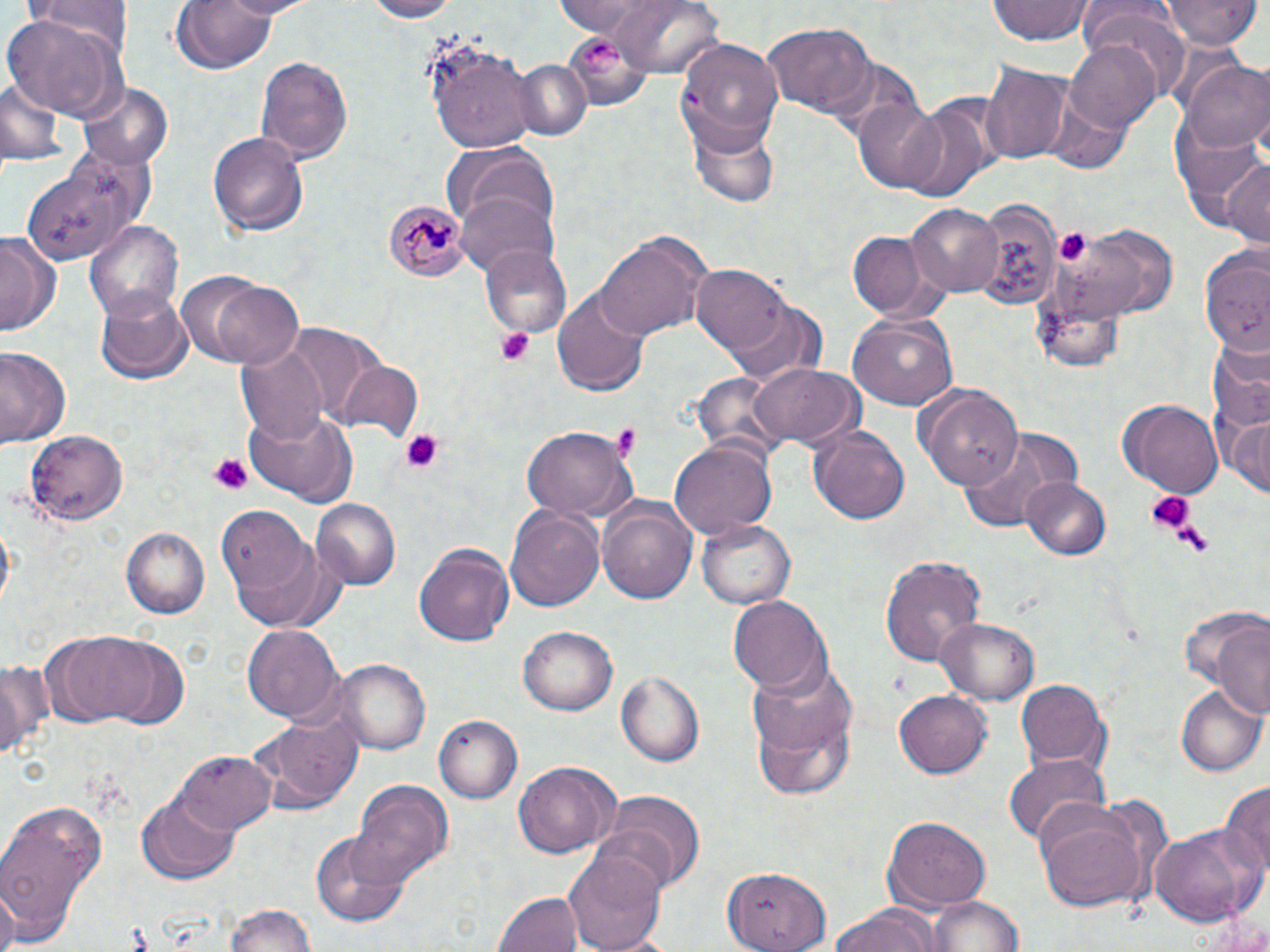
Summary:
  - Coordinate format: approximate bounding boxes as (x1,y1)-(x2,y2) corner pairs in pixels
  - Uninfected red blood cell locations: (29,0)-(128,58), (169,0)-(283,76), (210,0)-(320,19), (358,0)-(458,22), (601,0)-(722,78), (1163,0)-(1260,50), (987,1)-(1096,47), (1077,6)-(1192,89), (7,17)-(127,119), (763,20)-(876,116), (1064,37)-(1163,134), (423,38)-(539,151), (676,38)-(784,156), (255,56)-(354,167), (518,60)-(589,141), (981,61)-(1071,165), (1183,62)-(1270,157), (0,76)-(61,167), (76,77)-(177,170), (852,98)-(949,193), (896,103)-(996,206), (1175,105)-(1268,238), (687,118)-(781,211), (206,128)-(309,236), (448,149)-(563,247), (20,154)-(156,264), (1220,157)-(1269,247), (456,191)-(558,278), (971,200)-(1062,310), (908,205)-(1003,296), (84,220)-(185,327), (1058,225)-(1180,320), (593,227)-(714,342), (848,230)-(932,319), (0,232)-(56,338), (1199,241)-(1270,353), (482,243)-(571,339), (692,266)-(793,355), (213,282)-(305,368), (553,286)-(651,395), (97,288)-(193,384), (722,300)-(827,382), (848,315)-(956,409), (275,323)-(386,422), (237,342)-(328,443), (0,347)-(71,451), (330,360)-(423,441), (748,364)-(864,451), (918,384)-(1025,491), (1123,398)-(1225,496), (241,405)-(359,506), (1224,411)-(1269,500), (805,421)-(909,526), (518,422)-(636,521), (958,428)-(1080,530), (25,429)-(131,524), (669,439)-(776,542), (1022,478)-(1111,561), (597,498)-(697,606), (310,499)-(401,590), (217,505)-(326,627), (505,506)-(605,614), (699,518)-(799,609), (120,525)-(211,617), (416,541)-(515,647), (879,554)-(985,665), (728,595)-(829,694), (1181,603)-(1267,705), (932,617)-(1040,704), (1213,624)-(1269,722), (245,625)-(342,723), (518,625)-(617,715), (48,630)-(162,725), (102,640)-(191,732), (0,658)-(52,762), (333,659)-(432,754), (746,659)-(857,794), (616,672)-(704,766), (1017,678)-(1107,768), (1176,685)-(1267,778), (893,690)-(992,778), (251,711)-(364,815), (434,715)-(521,804), (175,750)-(276,832), (1005,757)-(1109,847), (513,763)-(617,857), (1222,780)-(1270,883), (350,783)-(452,890), (598,791)-(704,894), (138,793)-(240,883), (1035,801)-(1156,913), (0,804)-(106,941), (883,818)-(992,909), (1147,823)-(1263,927), (312,829)-(410,927), (562,846)-(665,952), (724,863)-(829,952), (0,884)-(18,952), (492,889)-(579,952), (925,892)-(1028,952), (220,903)-(318,952), (824,905)-(939,952), (1198,906)-(1269,950)
  - Platelet locations: (582,41)-(626,77), (1062,231)-(1090,266), (495,326)-(536,365), (398,428)-(447,474), (617,428)-(639,459), (208,453)-(252,492), (1144,490)-(1194,535)
  - Plasmodium malariae-infected red blood cell locations: (385,200)-(471,283)
  - Slide-level diagnosis: Plasmodium malariae
  - Image size: 1270×952 pixels
  - Field of view: single
  - Magnification: 1000x
  - Modality: light microscopy
  - Preparation: thin blood smear
  - Stain: May-Grünwald-Giemsa